Assess the morphology of the erythrocytes.
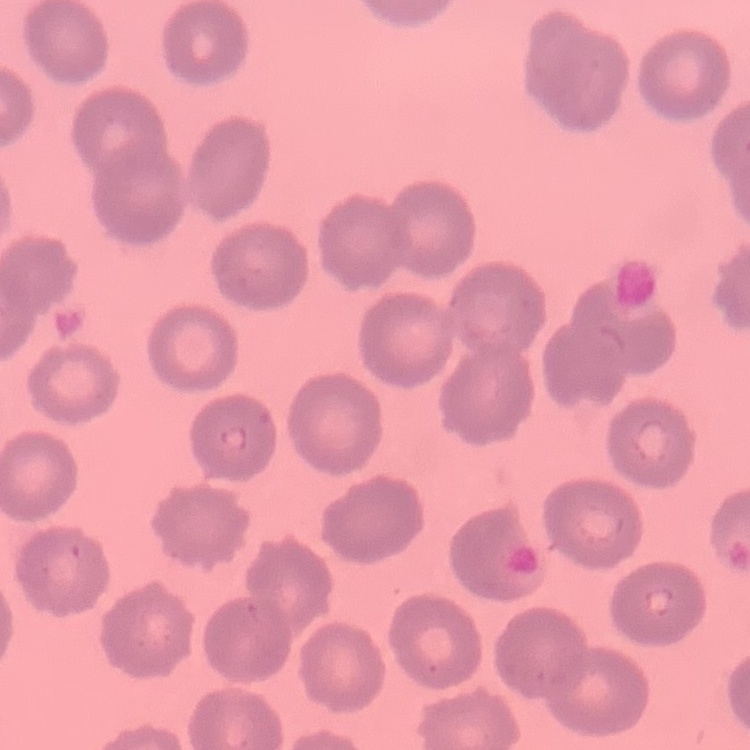

No rouleaux formation.

Field's or Giemsa stain. One tile cut from a larger photomicrograph. Thin blood film.